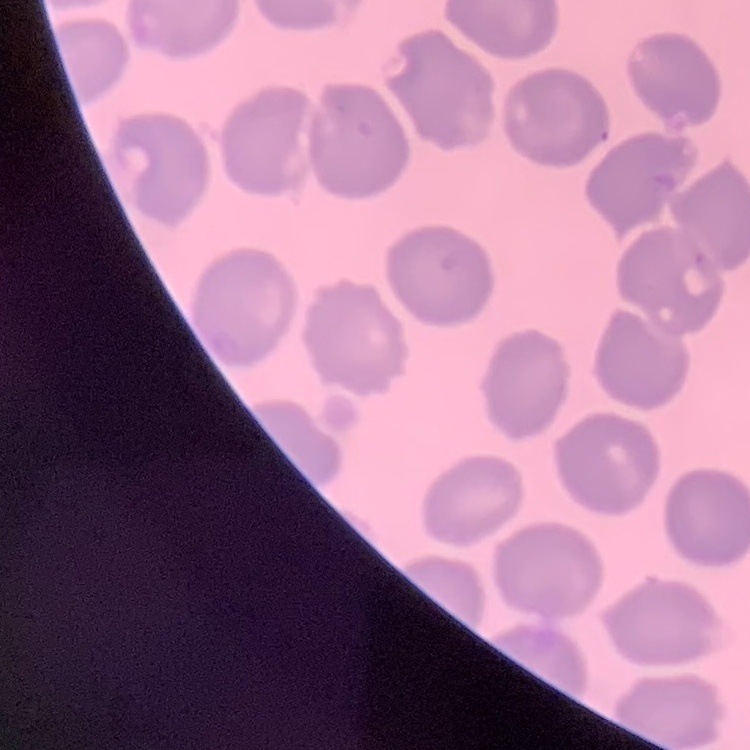
Summary:
  - Red blood cell morphology: no rouleaux formation
  - Stain: Field's or Giemsa
  - Image type: square crop of a larger photomicrograph
  - Preparation: thin blood film